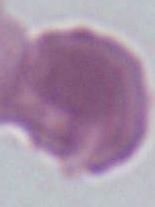
modality = micrograph
magnification = 1000x
identification = red blood cell